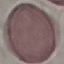

Result: no malaria parasites seen. Acquired by smartphone through the microscope eyepiece. Giemsa-stained preparation. Thin smear of blood. Cell patch, automatically extracted from a larger field of view and resized to 64 × 64 pixels.